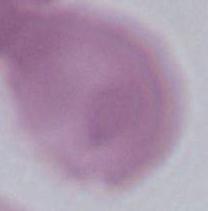

A red blood cell is shown. Captured at 1000x magnification. Photomicrograph.